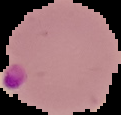

Summary:
  - Image type: segmented cell region on a black background
  - Malaria status: parasitized
  - Preparation: thin blood smear
  - Image size: 121×115 pixels